Classify this cell by malaria status.
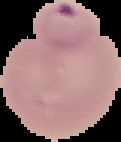

It is parasitized.

Summary:
  - Image type: cell region segmented out of the field of view; surrounding area masked to black
  - Image size: 121×142 pixels
  - Preparation: thin blood smear